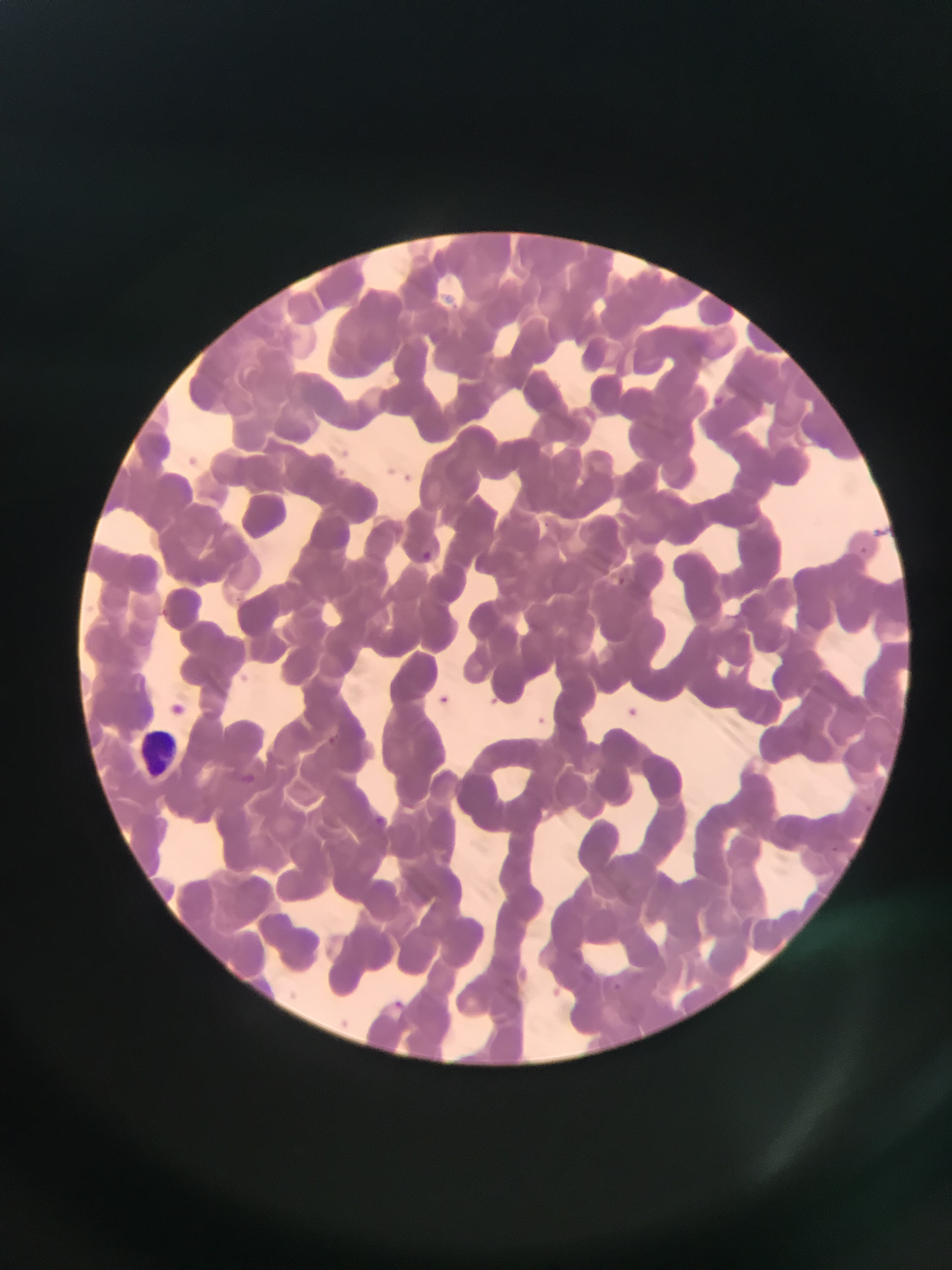 Approximate bounding boxes as (left, top, right, bottom) in pixels. Malaria parasite locations: (710, 394, 727, 410), (859, 544, 876, 566), (420, 545, 432, 559), (618, 574, 632, 596), (435, 696, 450, 706), (373, 811, 392, 825), (612, 980, 627, 992), (386, 994, 408, 1013). Leukocyte locations: (129, 726, 182, 786). Sample from Ghana. Single field of view. Image is 952×1270 pixels. Thin blood film. Mobile-phone photograph taken through the microscope.